Classify this cell by malaria status.
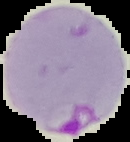

It is parasitized.

image type = segmented cell region on a black background
image size = 130×142 pixels
preparation = thin blood smear